Classify this cell by malaria status.
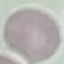

It is uninfected.

Photographed with a smartphone camera at the microscope eyepiece. Giemsa-stained preparation. Thin blood smear. Automatically extracted cell patch, resized to 64 × 64 pixels.